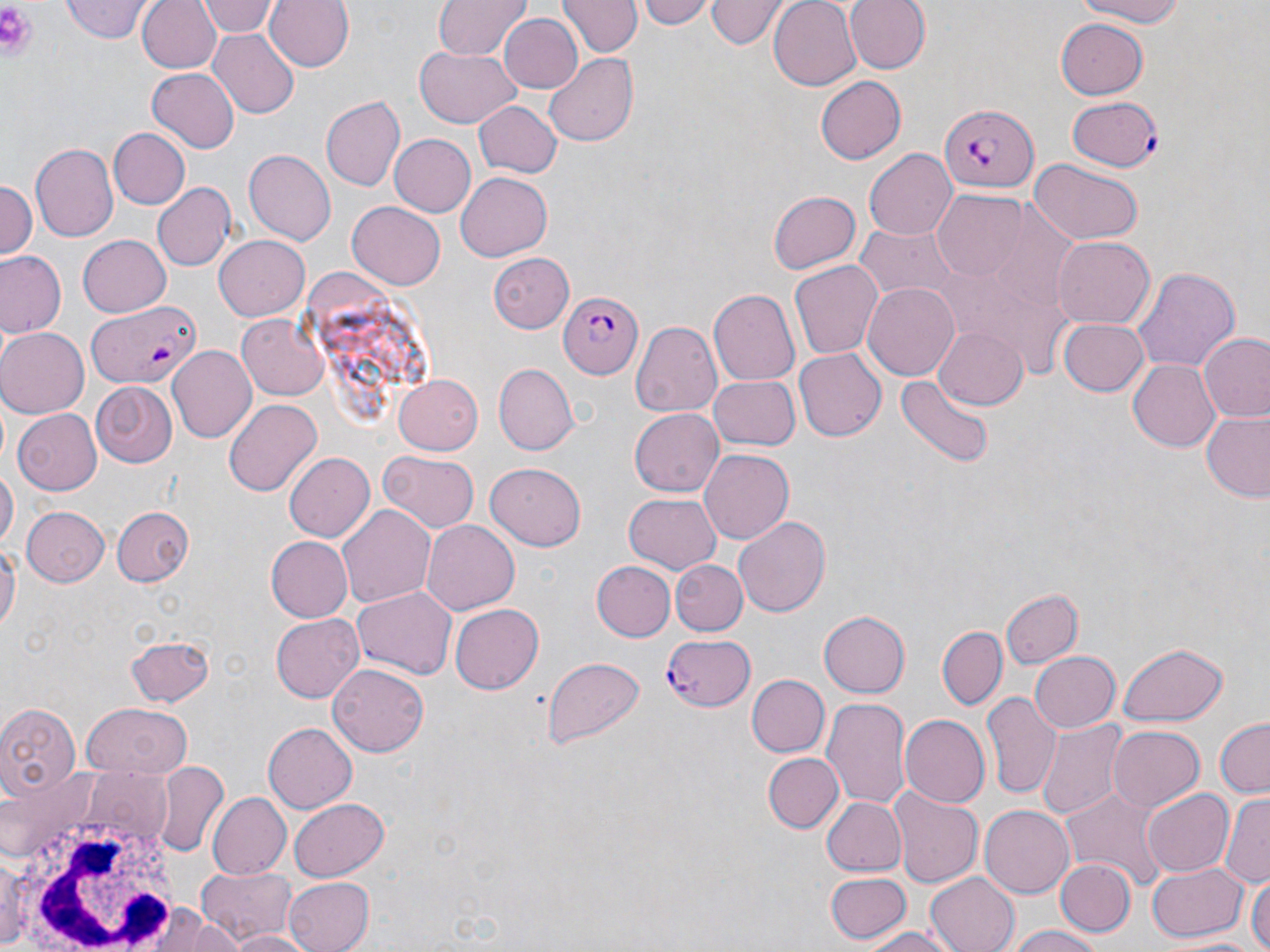

slide-level diagnosis = Plasmodium falciparum
preparation = thin blood smear
Plasmodium falciparum-infected red blood cell locations = approximate bounding boxes as named x1/y1/x2/y2 corners in pixels: (x1=1068, y1=96, x2=1161, y2=172), (x1=941, y1=104, x2=1038, y2=193), (x1=558, y1=291, x2=640, y2=377), (x1=87, y1=300, x2=201, y2=389), (x1=659, y1=632, x2=770, y2=720)
field of view = single
white blood cell locations = approximate bounding boxes as named x1/y1/x2/y2 corners in pixels: (x1=11, y1=796, x2=184, y2=952)
image size = 1270×952 pixels
uninfected red blood cell locations = approximate bounding boxes as named x1/y1/x2/y2 corners in pixels: (x1=138, y1=0, x2=223, y2=74), (x1=200, y1=0, x2=286, y2=73), (x1=201, y1=0, x2=278, y2=37), (x1=264, y1=0, x2=354, y2=73), (x1=433, y1=0, x2=533, y2=61), (x1=561, y1=0, x2=640, y2=58), (x1=636, y1=0, x2=712, y2=29), (x1=707, y1=0, x2=782, y2=49), (x1=769, y1=0, x2=863, y2=91), (x1=844, y1=0, x2=929, y2=75), (x1=1071, y1=0, x2=1194, y2=26), (x1=61, y1=2, x2=152, y2=43), (x1=498, y1=12, x2=582, y2=93), (x1=1057, y1=17, x2=1149, y2=100), (x1=209, y1=30, x2=301, y2=117), (x1=416, y1=44, x2=519, y2=127), (x1=546, y1=53, x2=639, y2=146), (x1=148, y1=70, x2=239, y2=151), (x1=815, y1=75, x2=906, y2=166), (x1=320, y1=96, x2=404, y2=190), (x1=472, y1=100, x2=561, y2=180), (x1=107, y1=128, x2=191, y2=210), (x1=390, y1=134, x2=476, y2=217), (x1=31, y1=144, x2=117, y2=240), (x1=867, y1=148, x2=956, y2=239), (x1=245, y1=149, x2=336, y2=245), (x1=1029, y1=161, x2=1143, y2=245), (x1=455, y1=172, x2=552, y2=260), (x1=0, y1=178, x2=37, y2=262), (x1=153, y1=184, x2=235, y2=270), (x1=768, y1=190, x2=861, y2=274), (x1=931, y1=193, x2=1025, y2=279), (x1=348, y1=200, x2=447, y2=289), (x1=854, y1=223, x2=959, y2=300), (x1=76, y1=234, x2=170, y2=316), (x1=214, y1=234, x2=311, y2=320), (x1=1052, y1=236, x2=1154, y2=329), (x1=955, y1=238, x2=1074, y2=383), (x1=1, y1=251, x2=65, y2=337), (x1=486, y1=252, x2=576, y2=330), (x1=789, y1=262, x2=883, y2=360), (x1=1133, y1=268, x2=1238, y2=371), (x1=862, y1=281, x2=960, y2=380), (x1=709, y1=288, x2=801, y2=385), (x1=238, y1=313, x2=332, y2=399), (x1=1057, y1=317, x2=1151, y2=396), (x1=630, y1=320, x2=722, y2=416), (x1=933, y1=326, x2=1029, y2=409), (x1=0, y1=327, x2=89, y2=417), (x1=1199, y1=333, x2=1270, y2=423), (x1=168, y1=346, x2=257, y2=442), (x1=793, y1=350, x2=885, y2=441), (x1=1130, y1=359, x2=1223, y2=451), (x1=492, y1=364, x2=576, y2=455), (x1=392, y1=374, x2=482, y2=456), (x1=708, y1=375, x2=799, y2=452), (x1=899, y1=375, x2=993, y2=468), (x1=90, y1=383, x2=178, y2=467), (x1=225, y1=400, x2=322, y2=496), (x1=629, y1=408, x2=723, y2=497), (x1=13, y1=410, x2=102, y2=493), (x1=1200, y1=410, x2=1270, y2=502), (x1=700, y1=448, x2=796, y2=543), (x1=284, y1=451, x2=375, y2=543), (x1=380, y1=452, x2=479, y2=532), (x1=485, y1=463, x2=587, y2=550), (x1=0, y1=464, x2=17, y2=551), (x1=624, y1=493, x2=721, y2=574), (x1=338, y1=502, x2=435, y2=605), (x1=110, y1=505, x2=195, y2=585), (x1=22, y1=506, x2=109, y2=586), (x1=734, y1=513, x2=831, y2=619), (x1=422, y1=519, x2=519, y2=615), (x1=264, y1=536, x2=353, y2=623), (x1=0, y1=537, x2=19, y2=636), (x1=591, y1=559, x2=675, y2=642), (x1=673, y1=559, x2=747, y2=635), (x1=352, y1=585, x2=455, y2=680), (x1=1000, y1=587, x2=1081, y2=669), (x1=450, y1=603, x2=543, y2=694), (x1=819, y1=609, x2=911, y2=696), (x1=268, y1=610, x2=364, y2=703), (x1=938, y1=626, x2=1007, y2=708), (x1=126, y1=634, x2=215, y2=705), (x1=1115, y1=641, x2=1229, y2=726), (x1=1027, y1=651, x2=1120, y2=733), (x1=545, y1=656, x2=646, y2=750), (x1=327, y1=664, x2=429, y2=756), (x1=745, y1=674, x2=828, y2=757), (x1=983, y1=691, x2=1058, y2=798), (x1=821, y1=698, x2=912, y2=811), (x1=0, y1=700, x2=80, y2=801), (x1=79, y1=703, x2=192, y2=777), (x1=899, y1=714, x2=989, y2=808), (x1=1214, y1=718, x2=1270, y2=797), (x1=1036, y1=719, x2=1127, y2=824), (x1=264, y1=722, x2=358, y2=812), (x1=1109, y1=725, x2=1205, y2=811), (x1=761, y1=752, x2=843, y2=834), (x1=153, y1=762, x2=228, y2=859), (x1=1061, y1=785, x2=1171, y2=891), (x1=1143, y1=788, x2=1234, y2=877), (x1=887, y1=789, x2=982, y2=887), (x1=206, y1=792, x2=290, y2=881), (x1=1220, y1=792, x2=1270, y2=883), (x1=819, y1=796, x2=907, y2=877), (x1=287, y1=797, x2=389, y2=881), (x1=978, y1=804, x2=1072, y2=900), (x1=0, y1=849, x2=35, y2=949), (x1=1053, y1=858, x2=1134, y2=937), (x1=1147, y1=862, x2=1246, y2=940), (x1=194, y1=866, x2=299, y2=944), (x1=926, y1=872, x2=1019, y2=952), (x1=825, y1=873, x2=910, y2=943), (x1=1249, y1=873, x2=1270, y2=952), (x1=281, y1=877, x2=373, y2=952), (x1=148, y1=899, x2=247, y2=949), (x1=1003, y1=925, x2=1109, y2=952), (x1=859, y1=927, x2=958, y2=951), (x1=228, y1=930, x2=312, y2=952), (x1=1164, y1=935, x2=1267, y2=951)
platelet locations = approximate bounding boxes as named x1/y1/x2/y2 corners in pixels: (x1=0, y1=0, x2=41, y2=64)
stain = May-Grünwald-Giemsa
magnification = 1000x
modality = light microscopy